Comment on the morphology of the red blood cells.
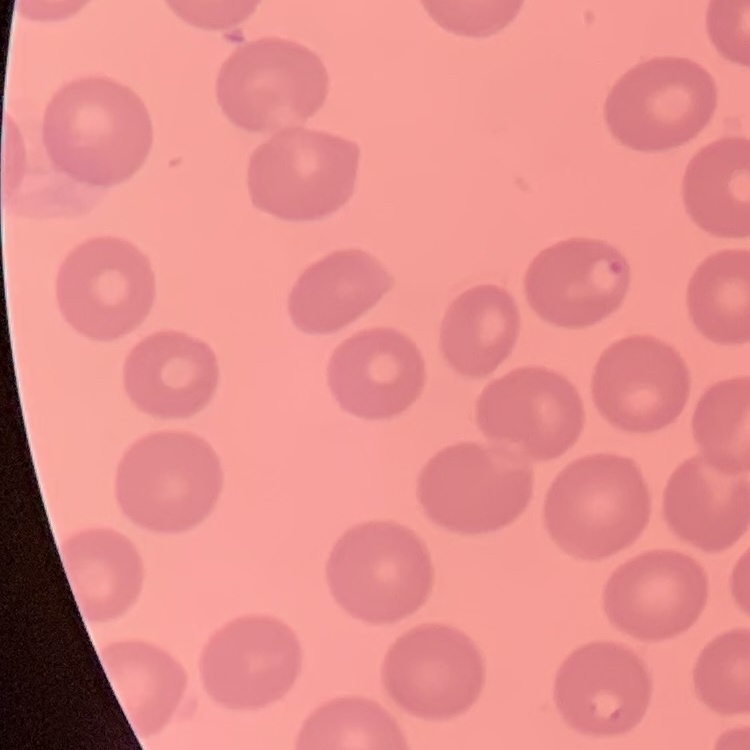
No rouleaux formation.

Summary:
  - Image type: one tile cut from a larger photomicrograph
  - Stain: Field's or Giemsa
  - Preparation: thin peripheral smear